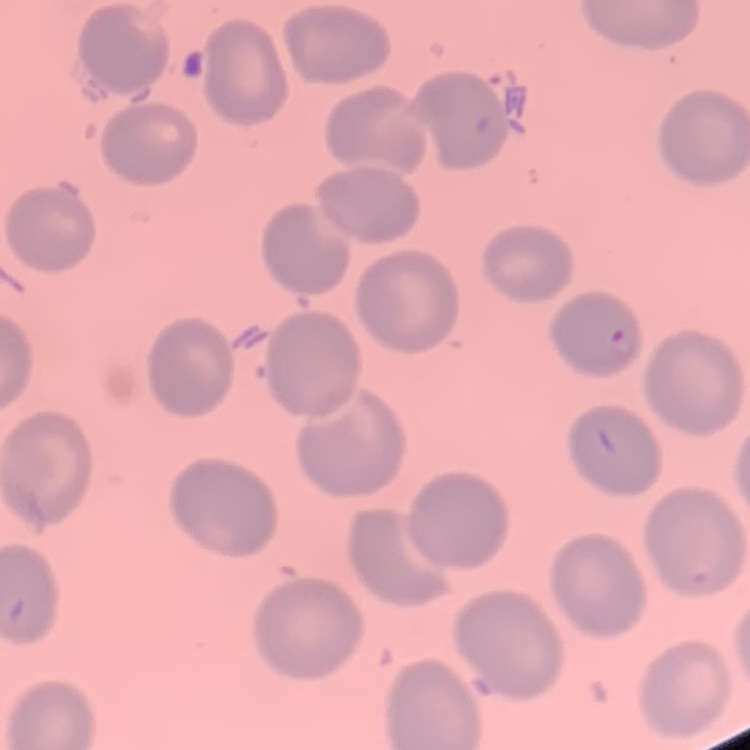
The erythrocytes show no rouleaux formation. Thin peripheral smear. Stained with either Field's or Giemsa. One tile cut from a larger photomicrograph.